Comment on the morphology of the erythrocytes.
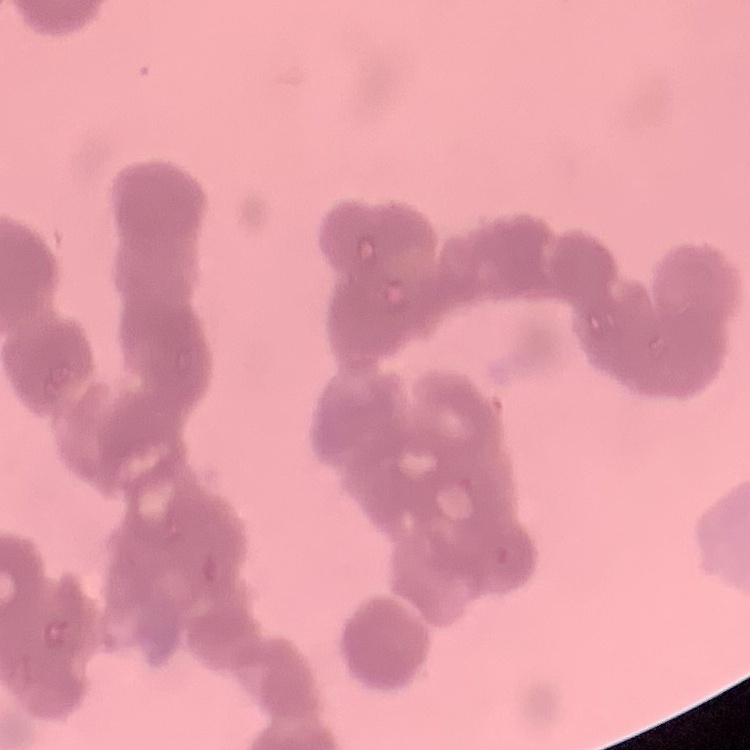

They show rouleaux formation.

Summary:
  - Stain: Field's or Giemsa
  - Image type: square crop of a larger photomicrograph
  - Preparation: thin blood film